Identify the parasite.
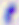
Toxoplasma gondii.

modality = photomicrograph
magnification = 400x